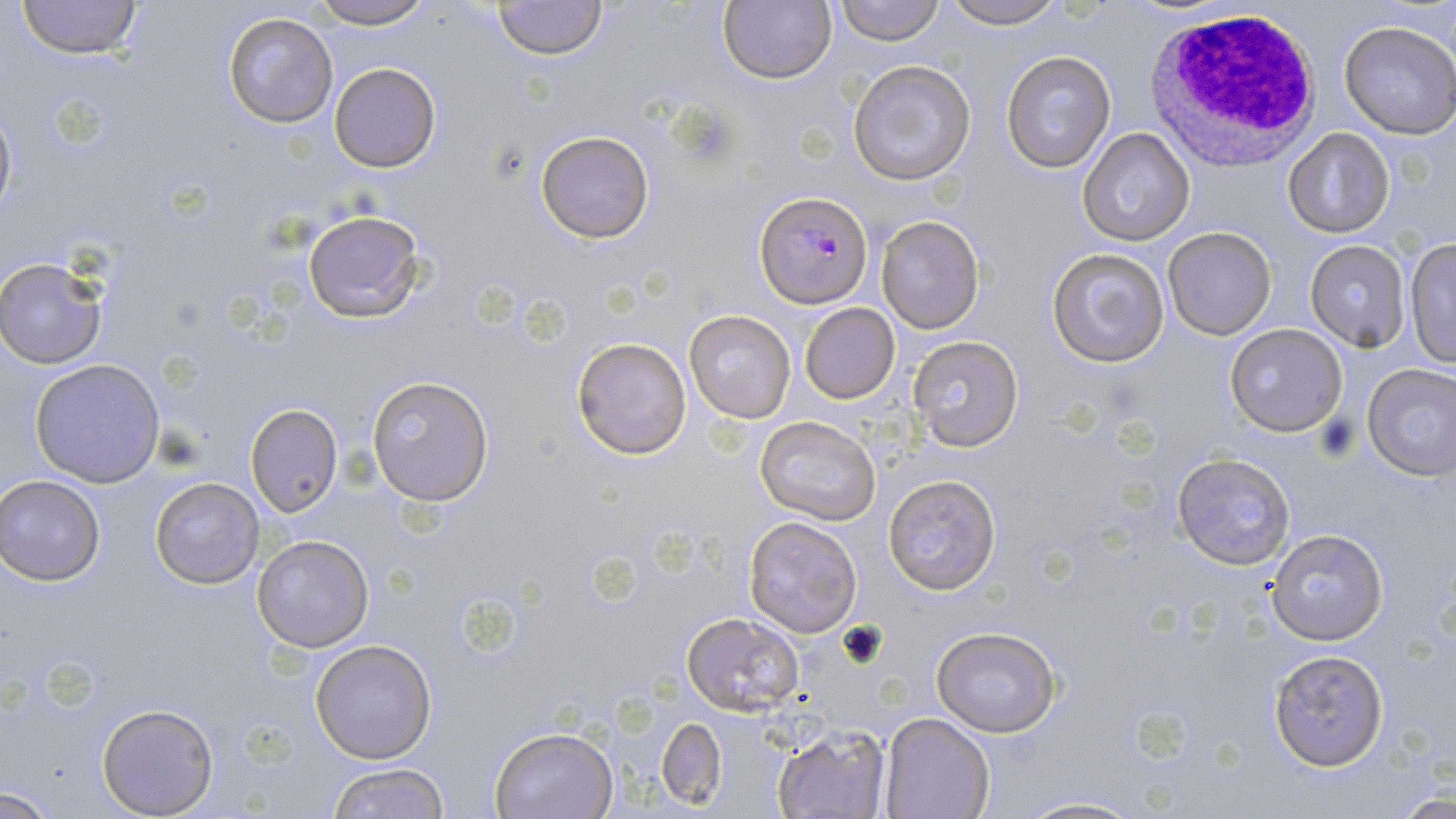
Approximate bounding boxes as (x1, y1, x2, y2) in pixels. White blood cell locations: (1143, 6, 1322, 167). Plasmodium falciparum-infected red blood cell locations: (756, 192, 874, 307). Uninfected red blood cell locations: (15, 0, 143, 61), (308, 0, 437, 29), (492, 0, 608, 60), (719, 0, 835, 86), (834, 0, 943, 45), (941, 0, 1068, 28), (222, 10, 341, 129), (1339, 21, 1456, 138), (1001, 50, 1116, 173), (848, 60, 976, 185), (329, 63, 441, 172), (0, 97, 17, 229), (1078, 128, 1195, 245), (1283, 129, 1394, 238), (536, 130, 654, 242), (301, 208, 427, 324), (875, 215, 986, 334), (1163, 227, 1276, 340), (1403, 238, 1456, 369), (1303, 240, 1409, 352), (1046, 247, 1171, 368), (1, 256, 109, 368), (800, 303, 901, 403), (684, 310, 795, 421), (1224, 323, 1348, 437), (907, 335, 1024, 451), (571, 336, 692, 459), (30, 359, 164, 488), (1362, 363, 1456, 480), (365, 375, 495, 506), (245, 403, 343, 516), (755, 416, 881, 525), (1171, 453, 1295, 571), (1, 474, 108, 585), (883, 474, 1002, 593), (150, 476, 265, 589), (744, 517, 862, 637), (1265, 528, 1389, 646), (253, 535, 374, 651), (680, 612, 805, 714), (929, 625, 1061, 737), (309, 639, 437, 764), (1267, 647, 1391, 771), (96, 703, 219, 817), (880, 713, 996, 819), (658, 715, 727, 810), (773, 723, 890, 819), (490, 726, 618, 818), (324, 761, 451, 819), (1, 785, 64, 816), (1011, 795, 1149, 819). Slide-level diagnosis: Plasmodium falciparum. Image is 1456×819 pixels. Captured at 1000x magnification. May-Grünwald-Giemsa-stained preparation. Thin blood film. Optical microscopy. Single field of view.